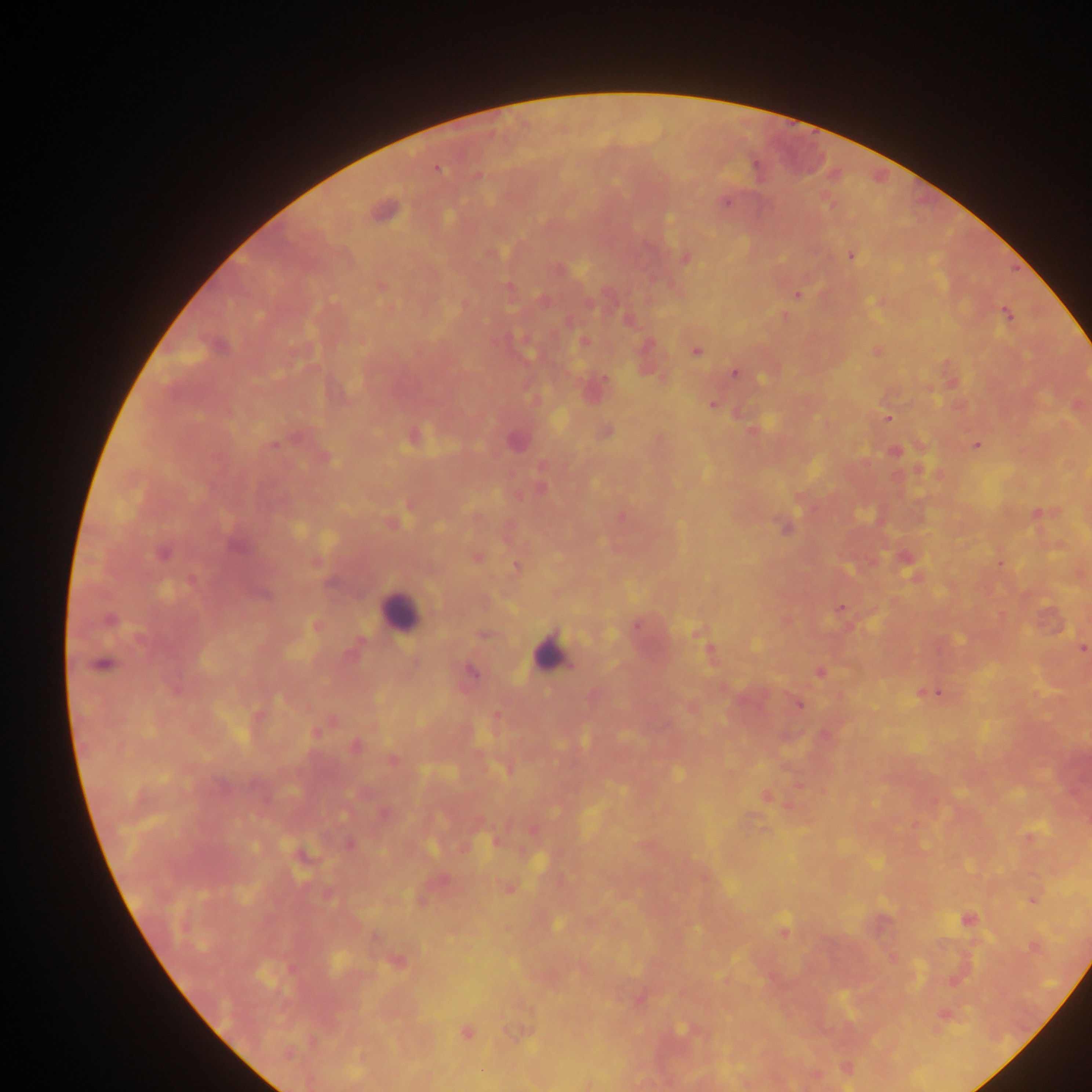
{
  "field_of_view": "single",
  "capture": "mobile-phone photograph through a microscope",
  "country": "Ghana",
  "plasmodium_parasite_locations": "approximate centers as [x, y] in pixels: [436, 169], [477, 175], [724, 200], [383, 211], [850, 254], [685, 257], [380, 285], [797, 295], [881, 301], [1006, 314], [783, 316], [627, 318], [584, 342], [695, 350], [877, 351], [647, 360], [734, 372], [952, 382], [593, 388], [712, 403], [1077, 404], [888, 417], [752, 430], [606, 431], [413, 436], [515, 441], [977, 445], [894, 451], [324, 458], [919, 468], [411, 504], [1037, 513], [621, 516], [392, 523], [785, 527], [163, 553], [476, 556], [904, 557], [316, 562], [1000, 562], [517, 565], [1079, 573], [915, 575], [262, 594], [840, 610], [109, 620], [786, 620], [316, 625], [636, 625], [698, 632], [484, 634], [1081, 648], [708, 650], [102, 664], [470, 671], [820, 672], [929, 691], [798, 704], [497, 715], [317, 732], [825, 735], [354, 746], [391, 760], [766, 795], [385, 814], [532, 830], [763, 830], [1029, 837], [496, 840], [350, 844], [302, 855], [439, 881], [507, 888], [1033, 899], [967, 919], [783, 931], [1034, 946], [891, 959], [396, 961], [638, 999], [944, 1014], [686, 1029], [519, 1031], [465, 1033], [846, 1068], [813, 1075], [587, 1084]",
  "preparation": "thick blood film",
  "image_size": "1092×1092 pixels",
  "leukocyte_locations": "approximate centers as [x, y] in pixels: [400, 613], [548, 654]"
}